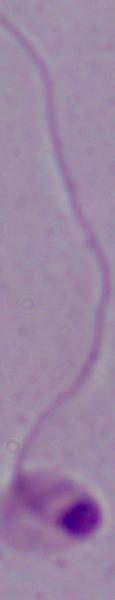
Summary:
  - Magnification: 1000x
  - Modality: photomicrograph
  - Identification: Leishmania